Report the malaria status of this cell.
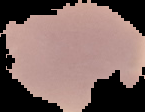
Uninfected.

Cell region segmented out of the field of view; the surrounding area is masked to black. From a thin blood smear. Image is 145×112 pixels.